Give the position of every Plasmodium parasite visible.
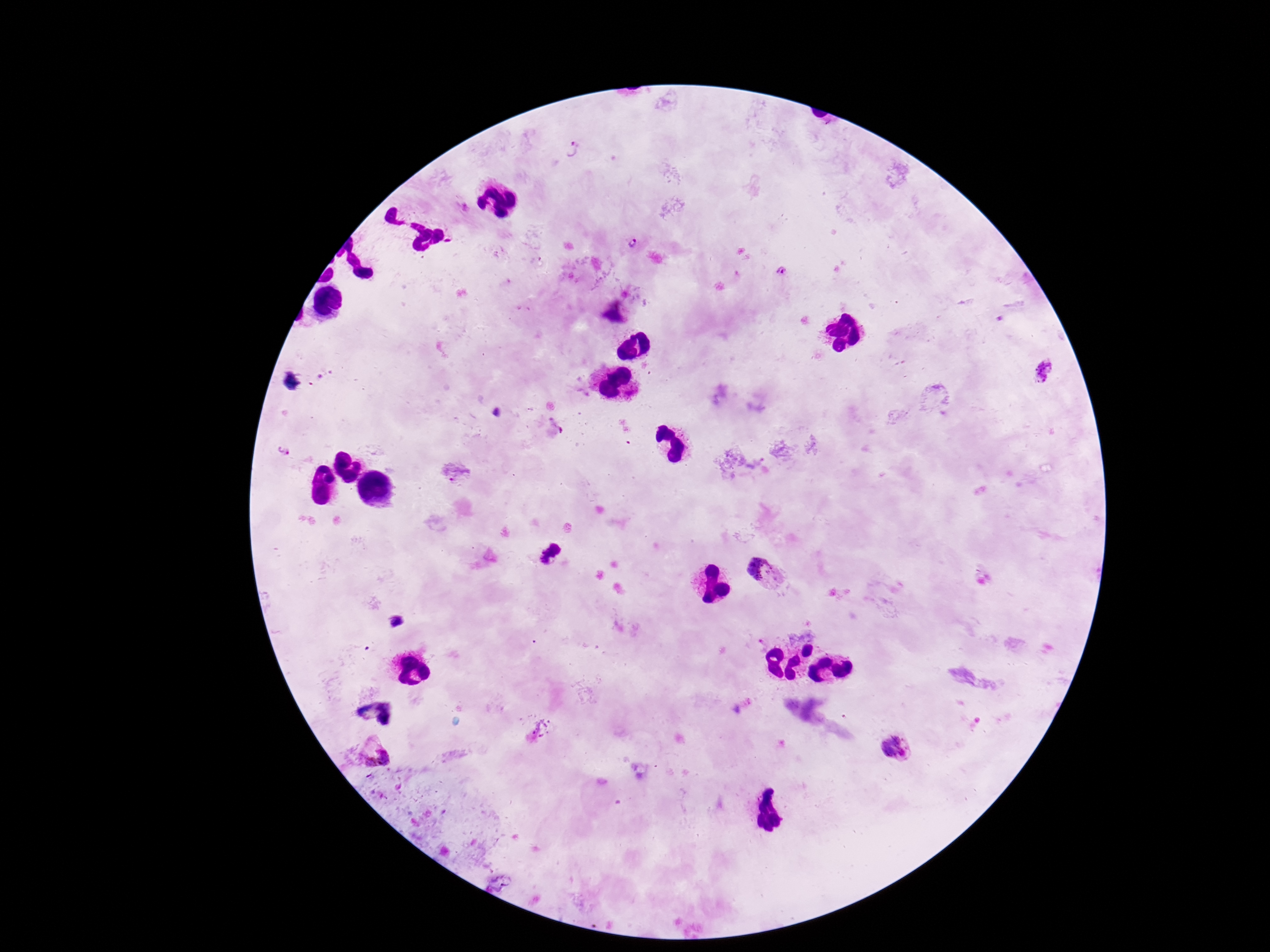
Approximate centers as {x, y} in pixels.
Plasmodium parasites: {568, 148}, {633, 244}, {781, 271}, {615, 310}, {1044, 373}, {283, 450}, {451, 472}, {551, 553}, {765, 572}, {398, 622}, {895, 747}, {374, 752}.

preparation = thick blood smear
field of view = one from this slide
patient malaria status = positive
capture = smartphone camera through the microscope eyepiece
image size = 1270×952 pixels
magnification = 100x
stain = Giemsa